Comment on the morphology of the red blood cells.
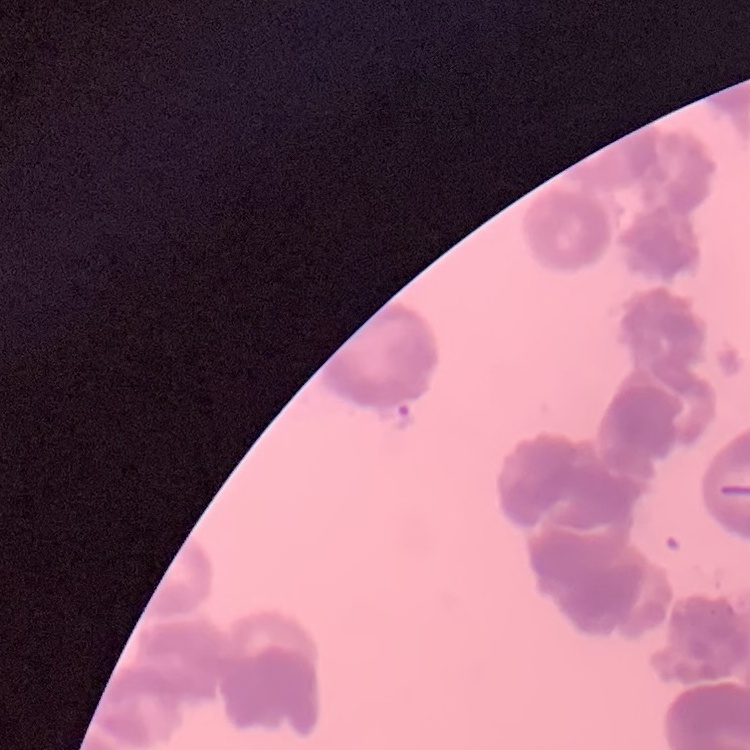

They show rouleaux formation.

Field's or Giemsa stain. One tile cut from a larger photomicrograph. Thin blood smear.